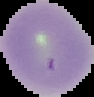 From a thin blood film. Segmented cell region on a black background. Image is 94×97 pixels. Malaria status: uninfected.